Locate every blood parasite and identify its species.
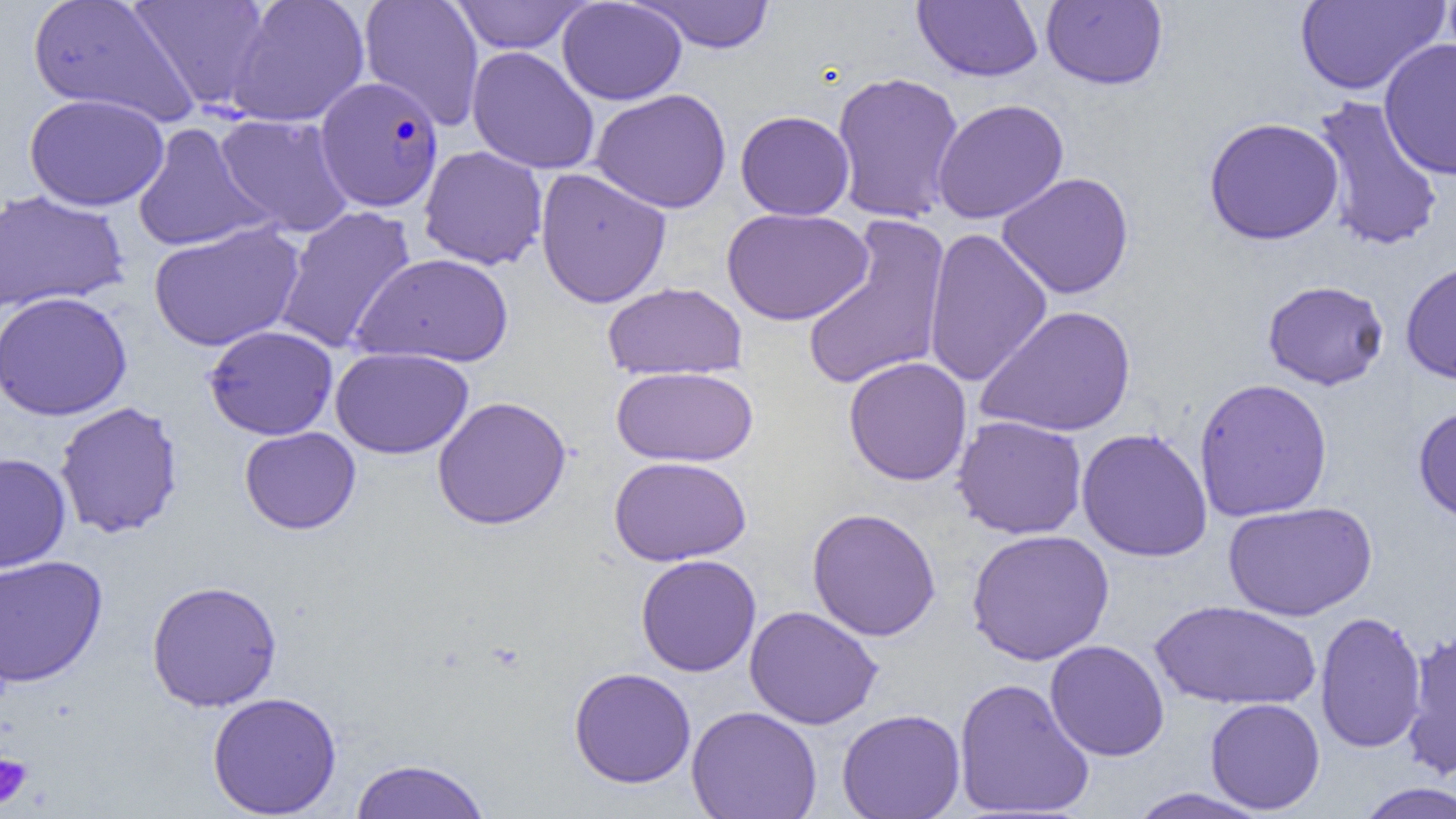

Approximate bounding boxes as [x1, y1, x2, y2] in pixels.
Plasmodium falciparum-infected red blood cells: [315, 76, 444, 212].
No Plasmodium ovale, Plasmodium malariae, Plasmodium vivax, Babesia divergens, or Trypanosoma brucei observed.

Uninfected red blood cell locations: [27, 0, 198, 127], [128, 0, 272, 110], [225, 0, 370, 127], [359, 0, 484, 130], [448, 0, 591, 54], [557, 0, 687, 105], [635, 0, 776, 53], [912, 0, 1044, 82], [1294, 0, 1449, 96], [1041, 1, 1168, 90], [1379, 38, 1456, 181], [466, 46, 601, 175], [830, 71, 965, 225], [590, 88, 732, 214], [24, 93, 169, 211], [1310, 95, 1446, 253], [931, 98, 1069, 224], [735, 110, 855, 220], [214, 113, 355, 237], [1203, 117, 1345, 245], [131, 122, 273, 252], [418, 145, 548, 270], [535, 167, 672, 309], [996, 172, 1135, 300], [0, 189, 129, 314], [273, 205, 417, 354], [722, 207, 873, 325], [801, 215, 951, 392], [148, 222, 305, 352], [922, 227, 1052, 388], [352, 253, 513, 368], [1400, 260, 1456, 385], [1262, 279, 1389, 390], [602, 282, 747, 381], [0, 291, 132, 421], [976, 305, 1136, 438], [204, 325, 338, 440], [331, 347, 474, 460], [843, 356, 972, 486], [611, 366, 759, 466], [1193, 377, 1333, 522], [432, 396, 571, 530], [54, 401, 184, 538], [1412, 403, 1456, 524], [952, 415, 1088, 540], [239, 426, 361, 534], [1076, 427, 1213, 562], [0, 452, 71, 572], [609, 456, 752, 566], [1223, 501, 1377, 621], [807, 507, 941, 641], [966, 529, 1115, 666], [0, 554, 108, 688], [635, 554, 762, 677], [146, 579, 283, 711], [1150, 600, 1321, 711], [744, 605, 883, 730], [1314, 611, 1427, 753], [1401, 629, 1456, 781], [1044, 640, 1170, 762], [568, 667, 696, 789], [953, 677, 1095, 818], [207, 691, 342, 817], [1205, 697, 1325, 814], [686, 705, 822, 819], [837, 708, 966, 819], [348, 758, 492, 818], [1354, 781, 1456, 819], [1125, 788, 1272, 818]. Platelet locations: [0, 753, 34, 809]. Slide-level diagnosis: Plasmodium falciparum. Image is 1456×819 pixels. Single field of view. Light microscopy. 1000x magnification. Thin blood film.